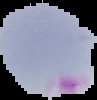

Result: Plasmodium parasites identified. Image is 97×100 pixels. Segmented cell region on a black background. From a thin blood film.